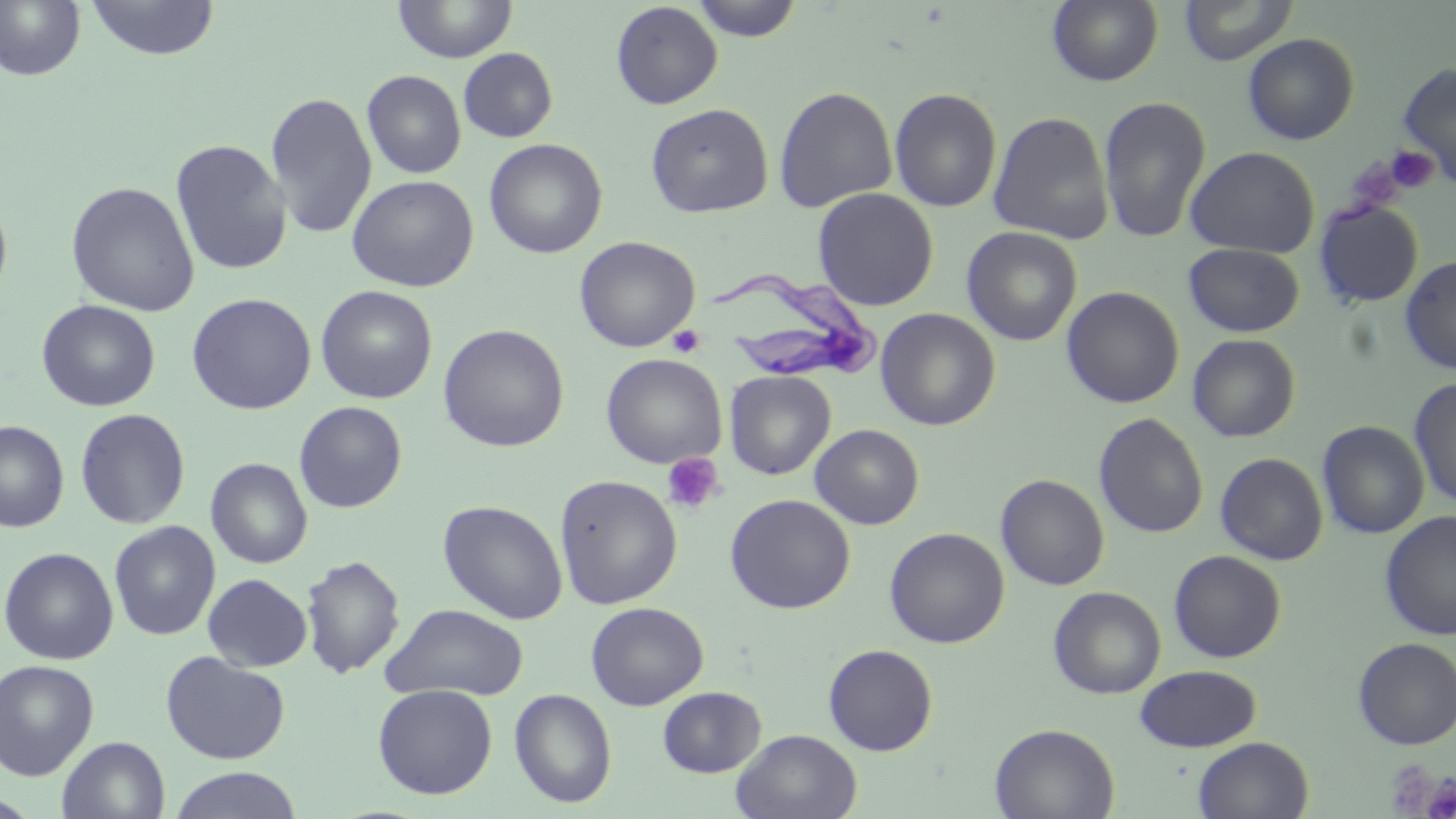
slide-level diagnosis = Trypanosoma brucei
modality = light microscopy
image size = 1456×819 pixels
Trypanosoma brucei locations = approximate bounding boxes as (x1, y1, x2, y2) in pixels: (708, 277, 883, 384)
platelet locations = approximate bounding boxes as (x1, y1, x2, y2) in pixels: (1386, 145, 1437, 193), (667, 325, 705, 357), (661, 452, 724, 514), (1385, 761, 1441, 816), (1423, 776, 1456, 819)
stain = May-Grünwald-Giemsa
preparation = thin blood smear
magnification = 1000x
field of view = one of a larger specimen
uninfected red blood cell locations = approximate bounding boxes as (x1, y1, x2, y2) in pixels: (85, 0, 220, 60), (393, 0, 517, 63), (689, 0, 803, 41), (1047, 0, 1164, 87), (1178, 0, 1299, 66), (0, 1, 86, 82), (610, 2, 723, 109), (1243, 33, 1360, 145), (458, 48, 558, 143), (1397, 62, 1456, 190), (362, 70, 466, 179), (773, 86, 897, 212), (889, 88, 1002, 212), (264, 91, 377, 240), (1097, 96, 1212, 243), (645, 103, 773, 218), (987, 111, 1114, 245), (484, 138, 607, 259), (170, 139, 291, 275), (1185, 146, 1320, 258), (347, 174, 479, 293), (65, 180, 200, 316), (812, 188, 938, 311), (0, 192, 13, 311), (1314, 200, 1424, 307), (961, 226, 1082, 346), (574, 235, 700, 353), (1184, 243, 1304, 337), (1400, 255, 1456, 375), (315, 285, 437, 404), (1061, 286, 1184, 408), (187, 293, 317, 414), (36, 299, 160, 411), (876, 308, 1000, 431), (438, 324, 569, 452), (1187, 334, 1301, 442), (601, 353, 726, 469), (725, 371, 836, 480), (1409, 377, 1456, 510), (294, 401, 407, 513), (75, 408, 191, 529), (1094, 412, 1209, 539), (0, 420, 69, 533), (1317, 420, 1429, 539), (810, 424, 924, 529), (1215, 452, 1328, 565), (205, 458, 313, 568), (995, 474, 1109, 590), (554, 475, 682, 609), (724, 493, 855, 614), (438, 500, 568, 625), (1379, 511, 1456, 640), (109, 520, 220, 640), (884, 527, 1010, 648), (0, 546, 119, 665), (1168, 550, 1286, 662), (300, 554, 405, 679), (202, 573, 313, 672), (1047, 586, 1166, 699), (585, 601, 709, 710), (381, 603, 529, 700), (1352, 637, 1456, 750), (823, 643, 938, 756), (160, 651, 291, 765), (0, 659, 100, 780), (1135, 664, 1262, 752), (372, 683, 497, 799), (657, 686, 766, 777), (509, 688, 617, 808), (989, 723, 1120, 818), (731, 729, 863, 819), (57, 736, 170, 819), (1193, 736, 1314, 819), (168, 767, 304, 819)